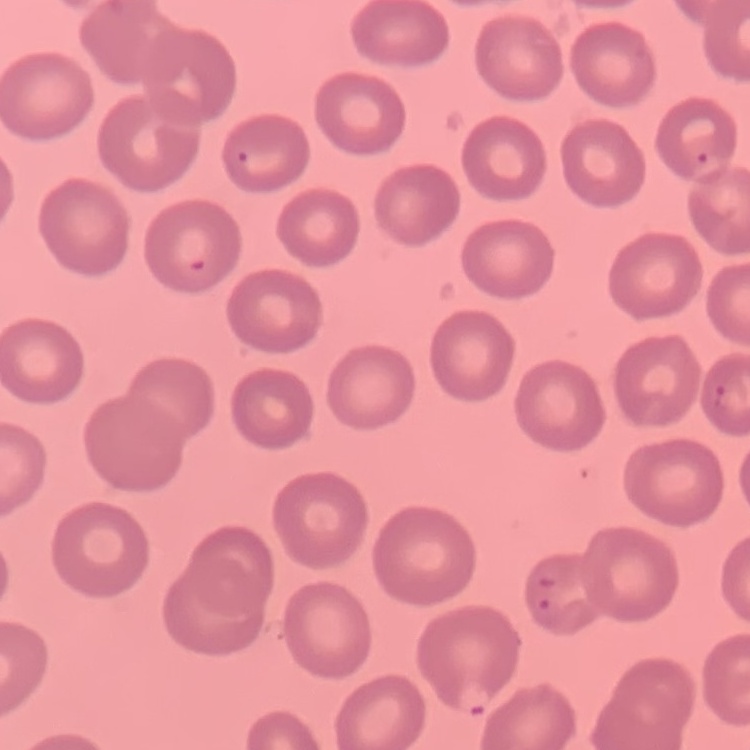

The erythrocytes show no rouleaux formation. One tile cut from a larger photomicrograph. Thin blood smear. Stained with either Field's or Giemsa.